Outline each blood parasite and name the species.
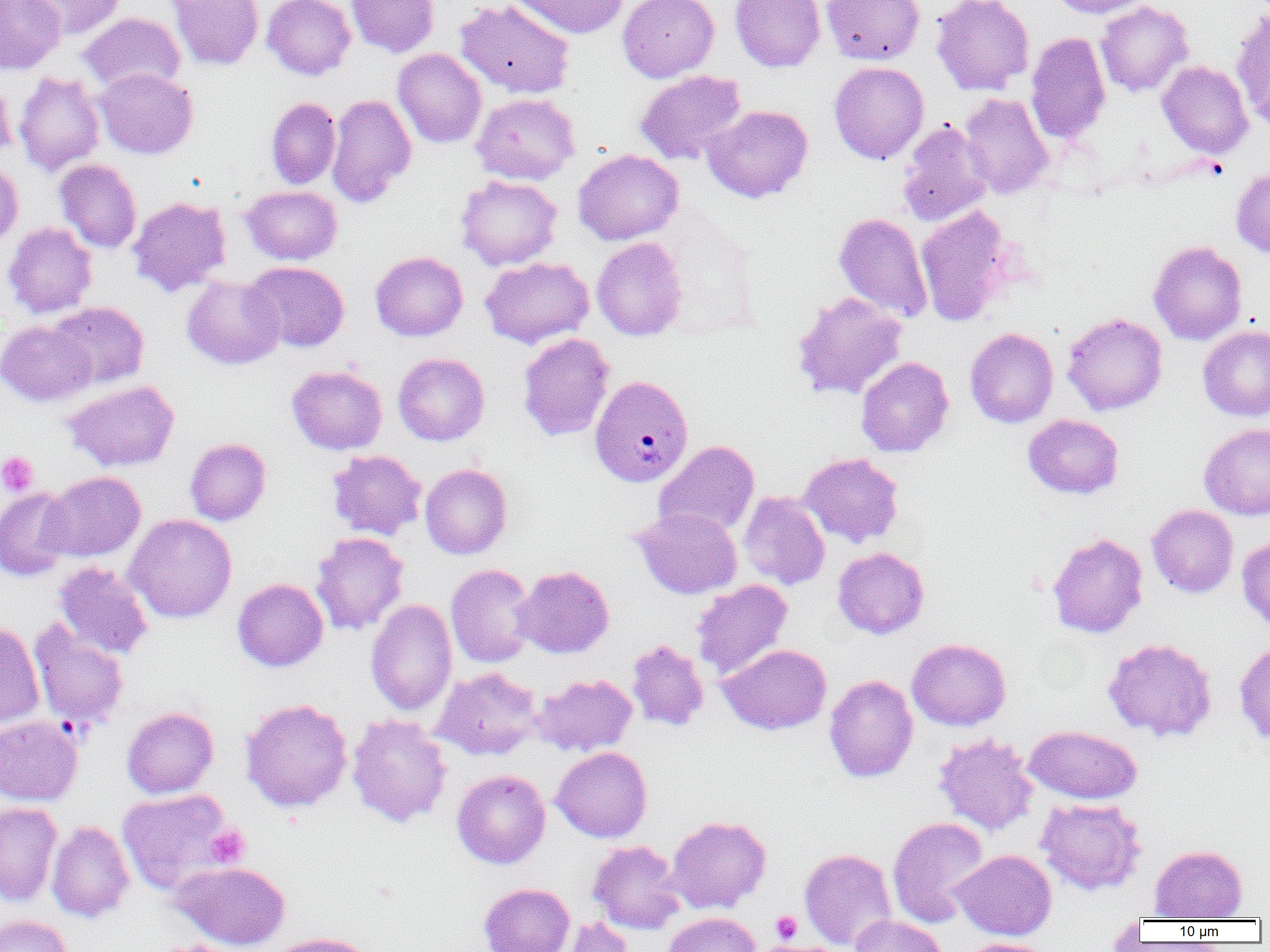
Approximate bounding boxes as (x1,y1)-(x2,y2) corner pairs in pixels.
Plasmodium vivax-infected red blood cells: (590,375)-(694,487).
No Plasmodium falciparum, Plasmodium ovale, Plasmodium malariae, Babesia divergens, or Trypanosoma brucei observed.

Summary:
  - Platelet locations: (0,451)-(38,497), (205,824)-(252,867), (771,911)-(803,944)
  - Uninfected red blood cell locations: (0,0)-(65,74), (22,0)-(125,41), (168,0)-(264,70), (262,0)-(355,80), (346,0)-(439,57), (455,0)-(575,99), (509,0)-(630,39), (618,0)-(719,82), (729,0)-(825,72), (822,0)-(925,65), (931,0)-(1034,95), (1048,0)-(1154,19), (1095,0)-(1194,97), (1230,6)-(1270,122), (79,13)-(185,93), (1026,32)-(1110,144), (393,48)-(487,148), (1157,60)-(1254,159), (829,61)-(928,165), (93,67)-(198,159), (634,70)-(747,164), (13,71)-(106,177), (0,77)-(17,164), (471,92)-(580,184), (326,93)-(416,208), (958,93)-(1054,199), (266,97)-(341,188), (702,105)-(814,203), (896,121)-(993,227), (573,150)-(684,245), (54,159)-(141,253), (0,161)-(24,250), (1231,165)-(1270,258), (455,174)-(562,271), (242,186)-(342,265), (128,196)-(231,296), (916,205)-(1015,326), (833,212)-(933,322), (3,221)-(98,319), (591,237)-(687,341), (1148,241)-(1247,345), (370,251)-(468,341), (480,257)-(594,348), (245,261)-(349,352), (181,275)-(285,370), (791,291)-(907,400), (46,301)-(149,389), (1062,312)-(1167,416), (0,321)-(95,406), (1197,325)-(1270,422), (965,327)-(1058,428), (517,333)-(614,441), (393,353)-(489,445), (856,356)-(953,457), (286,364)-(387,454), (62,380)-(180,472), (1024,414)-(1124,499), (1199,423)-(1270,520), (185,438)-(271,525), (655,440)-(760,537), (327,449)-(426,540), (799,452)-(904,548), (420,463)-(512,559), (41,470)-(146,562), (0,488)-(76,581), (739,491)-(830,590), (1146,504)-(1238,598), (631,507)-(742,599), (125,513)-(237,623), (311,531)-(409,635), (1047,532)-(1148,639), (1237,536)-(1270,633), (832,547)-(929,639), (53,561)-(154,660), (445,564)-(536,668), (514,565)-(614,658), (232,578)-(328,672), (691,579)-(793,680), (365,599)-(457,717), (29,619)-(129,732), (0,621)-(44,730), (1102,637)-(1218,742), (907,638)-(1010,731), (626,639)-(709,731), (1235,641)-(1270,747), (717,643)-(832,734), (432,666)-(543,760), (533,673)-(637,756), (824,674)-(918,783), (240,698)-(353,813), (121,707)-(218,798), (347,714)-(452,828), (0,715)-(83,806), (1024,725)-(1142,805), (932,732)-(1039,836), (551,747)-(652,842), (452,763)-(649,855), (452,769)-(551,869), (116,788)-(236,897), (1035,798)-(1147,896), (0,801)-(62,906), (666,815)-(771,913), (887,816)-(990,927), (47,820)-(135,923), (588,840)-(686,934), (1149,844)-(1247,921), (799,848)-(897,951), (951,849)-(1056,940), (170,861)-(291,951), (479,882)-(575,952), (663,912)-(760,952), (0,914)-(73,952), (850,914)-(948,952), (560,917)-(634,952), (263,932)-(378,952), (959,938)-(1056,952), (151,940)-(251,952)
  - Slide-level diagnosis: Plasmodium vivax
  - Magnification: 1000x
  - Field of view: one of a larger specimen
  - Modality: light microscopy
  - Preparation: thin blood smear
  - Image size: 1270×952 pixels